Name the cell type shown.
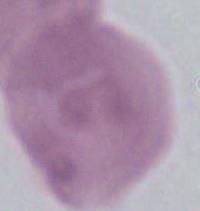

This is an erythrocyte.

1000x magnification. Photomicrograph.